Locate every Plasmodium malariae-infected red blood cell.
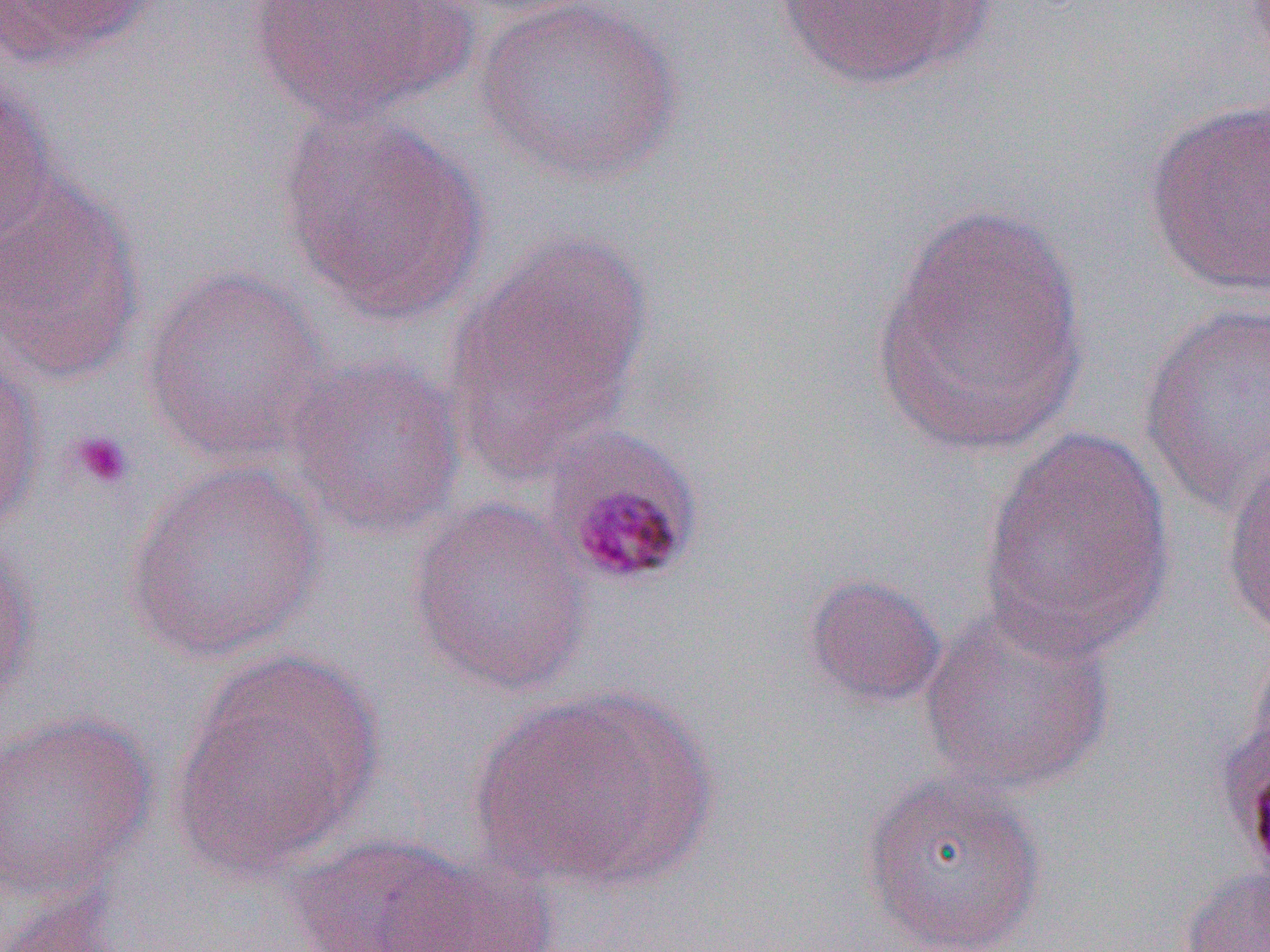

Approximate bounding boxes as (x1,y1)-(x2,y2) corner pairs in pixels.
Plasmodium malariae-infected red blood cells: (538,423)-(706,590).

slide-level diagnosis = Plasmodium malariae
modality = optical microscopy
magnification = 1000x
preparation = thin blood smear
uninfected red blood cell locations = approximate bounding boxes as (x1,y1)-(x2,y2) corner pairs in pixels: (244,0)-(474,125), (436,0)-(608,19), (473,0)-(685,186), (770,0)-(994,91), (0,1)-(157,67), (0,77)-(58,245), (1143,99)-(1270,297), (278,106)-(492,325), (0,176)-(146,381), (871,200)-(1089,458), (444,233)-(654,475), (143,266)-(329,466), (1137,302)-(1270,519), (0,346)-(45,534), (285,353)-(467,541), (979,425)-(1176,663), (1221,450)-(1270,642), (125,461)-(326,664), (407,497)-(594,696), (0,535)-(41,712), (802,573)-(947,708), (918,603)-(1116,797), (1244,638)-(1270,783), (171,650)-(383,877), (466,685)-(717,892), (0,711)-(158,902), (860,771)-(1048,952), (283,834)-(483,952), (381,851)-(559,951), (1178,865)-(1270,952), (4,889)-(130,952)
image size = 1270×952 pixels
platelet locations = approximate bounding boxes as (x1,y1)-(x2,y2) corner pairs in pixels: (66,429)-(134,491)
field of view = single